Classify this cell by malaria status.
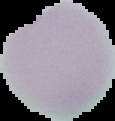

Uninfected.

Segmented cell region on a black background. From a thin blood film. Image is 115×121 pixels.